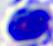
{
  "magnification": "400x",
  "identification": "white blood cell",
  "modality": "micrograph"
}